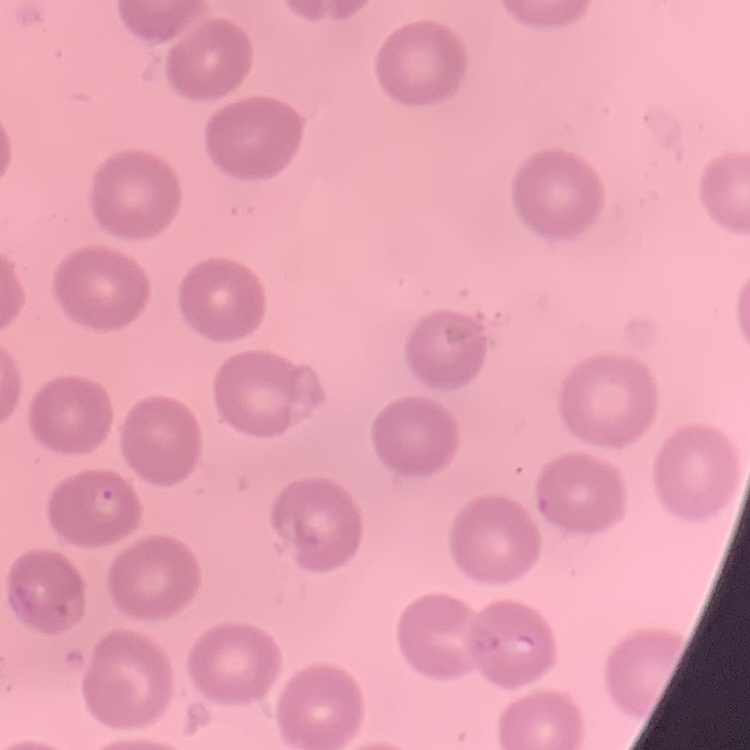

Summary:
  - Red blood cell morphology: no rouleaux formation
  - Image type: one tile cut from a larger photomicrograph
  - Preparation: thin peripheral smear
  - Stain: Field's or Giemsa